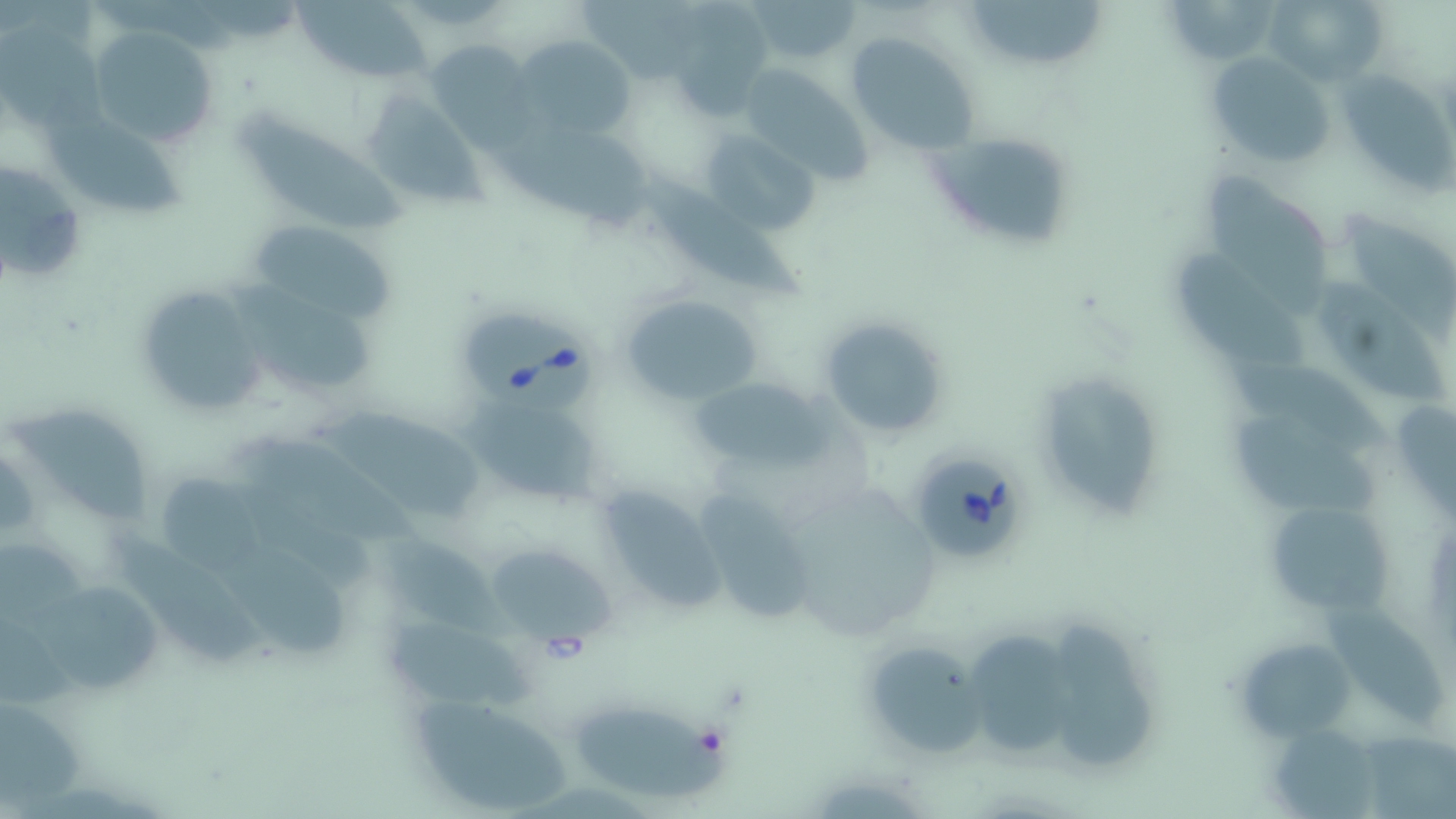

Approximate bounding boxes as (x1, y1, x2, y2) in pixels. Uninfected red blood cell locations: (295, 0, 434, 85), (747, 0, 863, 66), (961, 0, 1103, 65), (1168, 0, 1271, 65), (1263, 0, 1386, 86), (583, 1, 706, 79), (680, 7, 771, 117), (0, 18, 108, 136), (88, 26, 217, 149), (845, 31, 982, 155), (514, 35, 632, 139), (427, 39, 534, 144), (1207, 53, 1333, 167), (738, 71, 872, 186), (1341, 71, 1456, 200), (364, 91, 486, 211), (38, 104, 184, 214), (245, 111, 415, 233), (499, 114, 662, 232), (699, 131, 819, 237), (932, 131, 1075, 248), (0, 157, 91, 288), (1207, 168, 1332, 315), (648, 177, 807, 299), (1344, 212, 1456, 340), (258, 223, 393, 317), (1166, 247, 1308, 372), (223, 275, 375, 387), (135, 281, 268, 417), (1315, 283, 1453, 410), (621, 293, 763, 405), (817, 315, 953, 442), (1228, 355, 1392, 456), (684, 373, 834, 476), (1051, 375, 1166, 520), (464, 387, 607, 513), (13, 398, 146, 522), (313, 398, 483, 518), (1230, 410, 1383, 518), (251, 435, 417, 544), (0, 441, 40, 546), (156, 472, 264, 579), (699, 485, 807, 621), (604, 486, 735, 612), (1266, 501, 1399, 611), (115, 523, 267, 667), (381, 530, 518, 649), (485, 542, 614, 645), (222, 546, 348, 660), (39, 579, 161, 694), (1326, 601, 1448, 730), (388, 619, 542, 712), (1052, 625, 1160, 763), (968, 627, 1078, 755), (1235, 638, 1356, 741), (867, 642, 991, 754), (411, 690, 577, 814), (4, 700, 88, 808), (573, 703, 736, 795), (1268, 730, 1375, 816). Babesia divergens-infected red blood cell locations: (464, 311, 602, 417), (905, 448, 1032, 565). Slide-level diagnosis: Babesia divergens. Captured at 1000x magnification. Optical microscopy. Image is 1456×819 pixels. One field of a larger specimen. May-Grünwald-Giemsa stain. Thin blood smear.